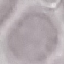
malaria_status: uninfected
preparation: thin blood smear
capture: smartphone camera at the microscope eyepiece
image_type: automatically extracted cell patch, resized to 64 × 64 pixels
stain: Giemsa